Assess this cell for malaria.
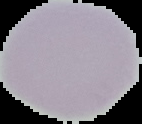
Uninfected.

{
  "preparation": "thin blood smear",
  "image_size": "142×124 pixels",
  "image_type": "segmented cell region on a black background"
}